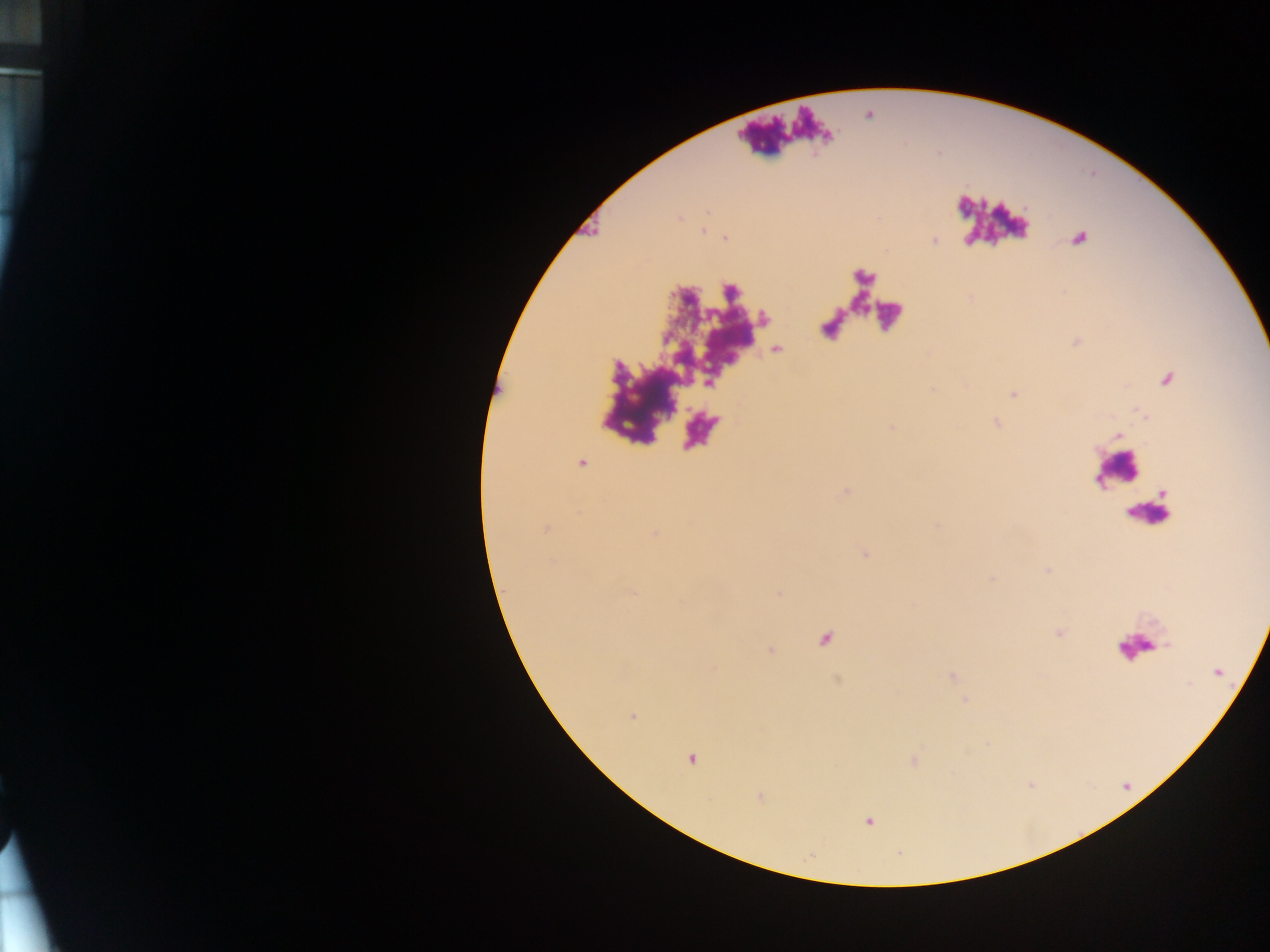

Approximate centers as x y in pixels. Leukocyte locations: 1117 471. Plasmodium parasite locations: 1167 381; 632 716; 691 760; 868 821. One field of view. Image is 1270×952 pixels. Sample from Ghana. Photographed through a microscope with a mobile-phone camera. Thick blood film.